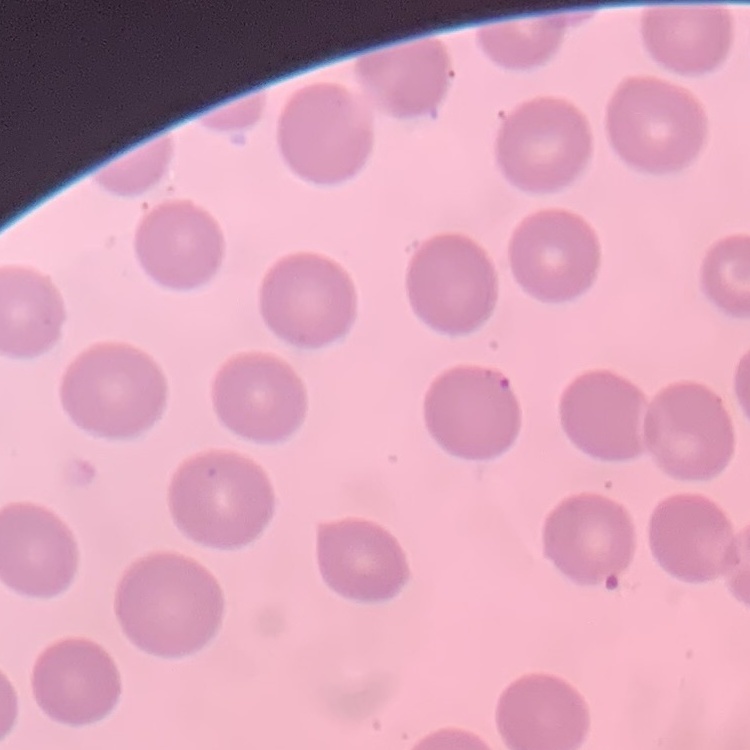
Summary:
  - Red blood cell morphology: no rouleaux formation
  - Image type: square crop of a larger photomicrograph
  - Preparation: thin blood smear
  - Stain: Field's or Giemsa